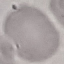
result: negative for malaria parasites
image_type: automatically extracted cell patch, resized to 64 × 64 pixels
preparation: thin blood smear
capture: smartphone camera at the microscope eyepiece
stain: Giemsa